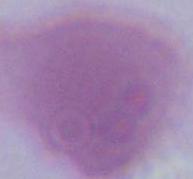 Photomicrograph. An erythrocyte is seen. Captured at 1000x magnification.